Name the parasite shown.
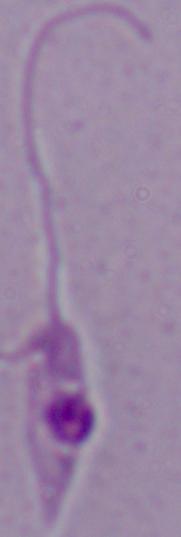

This is Leishmania.

Photomicrograph. Captured at 1000x magnification.